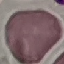
Result: no malaria parasites seen. Giemsa-stained preparation. Acquired by smartphone through the microscope eyepiece. Thin smear of blood. Cell patch, automatically extracted from a larger field of view and resized to 64 × 64 pixels.